Classify this cell by malaria status.
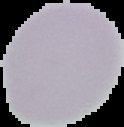
Uninfected.

image type = segmented cell region on a black background
image size = 124×127 pixels
preparation = thin blood film